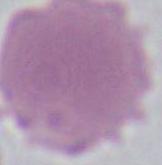

identification = red blood cell
modality = micrograph
magnification = 1000x